Report the malaria status of this cell.
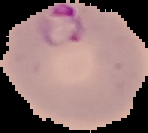

Parasitized.

image_size: 148×133 pixels
image_type: segmented cell region with the area outside set to black
preparation: thin blood smear